State the blood parasite species.
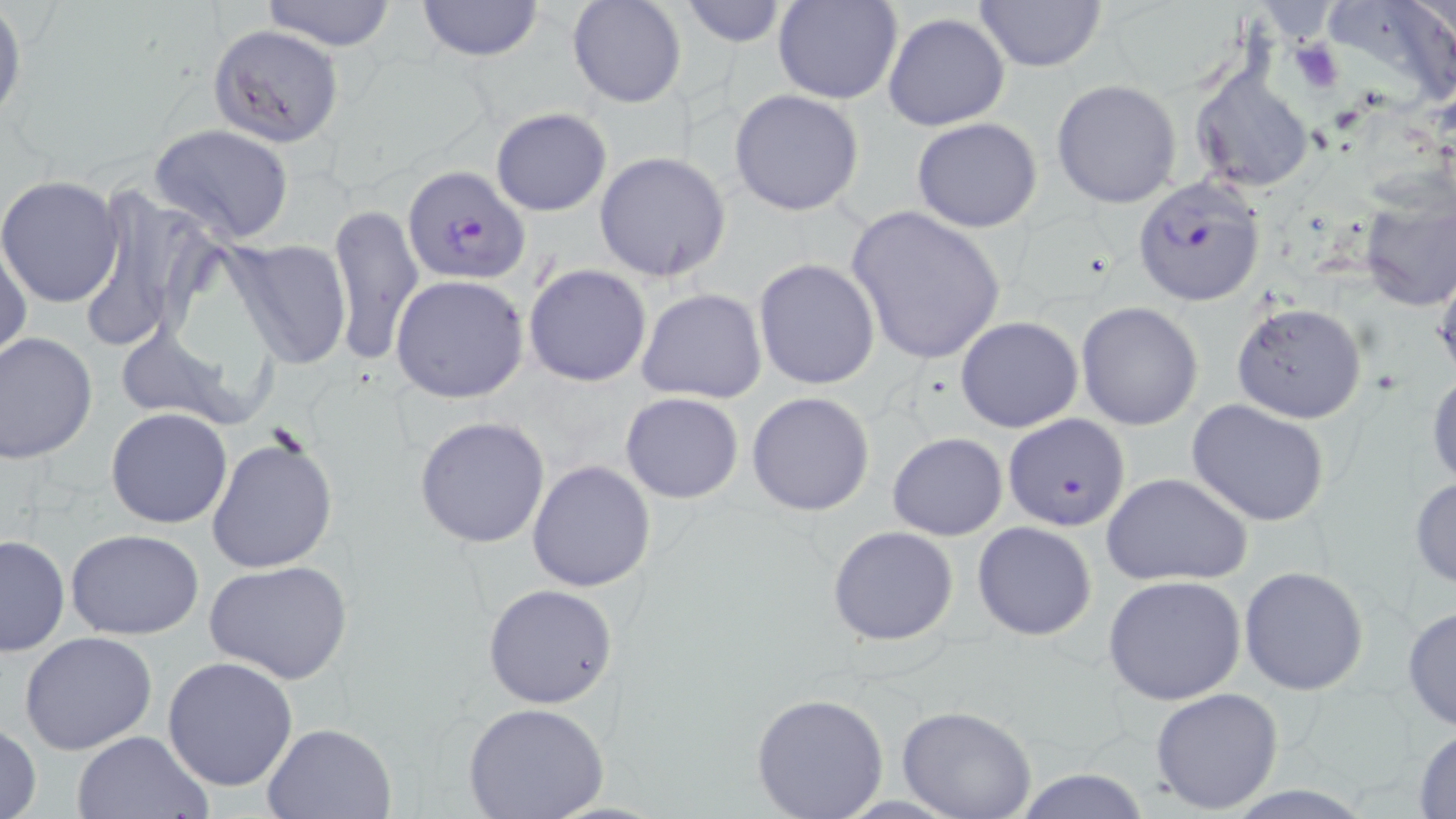
Plasmodium falciparum.

Approximate bounding boxes as (x1,y1)-(x2,y2) corner pairs in pixels. Plasmodium falciparum-infected red blood cell locations: (403,164)-(531,287), (1131,175)-(1267,306), (1002,412)-(1131,531). Platelet locations: (1289,41)-(1344,93). Uninfected red blood cell locations: (258,0)-(399,50), (413,0)-(546,63), (567,0)-(688,109), (773,0)-(903,104), (1324,0)-(1456,107), (679,1)-(788,48), (973,1)-(1107,73), (0,5)-(25,123), (883,12)-(1010,131), (208,24)-(343,147), (1188,63)-(1316,194), (1051,79)-(1182,208), (727,88)-(865,216), (490,106)-(612,216), (912,118)-(1043,233), (150,122)-(296,244), (593,151)-(731,282), (0,176)-(125,306), (76,185)-(221,354), (1355,190)-(1456,311), (328,203)-(424,366), (846,205)-(1007,366), (0,238)-(31,363), (223,238)-(354,368), (753,258)-(880,392), (1433,262)-(1455,382), (523,263)-(652,387), (391,274)-(529,402), (637,287)-(767,404), (1232,301)-(1366,424), (1076,302)-(1203,430), (954,316)-(1085,432), (113,325)-(251,429), (0,331)-(99,464), (1427,367)-(1456,490), (745,391)-(875,517), (620,393)-(744,505), (1187,399)-(1332,528), (105,408)-(233,529), (414,415)-(551,549), (888,431)-(1008,540), (205,434)-(339,575), (526,460)-(657,593), (1102,472)-(1252,588), (1410,475)-(1456,589), (973,522)-(1096,641), (826,525)-(960,646), (65,530)-(204,640), (0,534)-(70,658), (205,561)-(353,684), (1239,565)-(1369,696), (1103,574)-(1246,705), (482,583)-(618,708), (1401,605)-(1456,733), (20,632)-(158,755), (163,657)-(299,792), (1151,687)-(1285,814), (750,692)-(890,818), (462,701)-(610,819), (897,706)-(1038,819), (0,721)-(43,819), (262,722)-(399,818), (1412,727)-(1456,816), (70,730)-(211,818), (1004,767)-(1154,819). Captured at 1000x magnification. Single field of view. Optical microscopy. May-Grünwald-Giemsa-stained preparation. Image is 1456×819 pixels. Thin blood film.